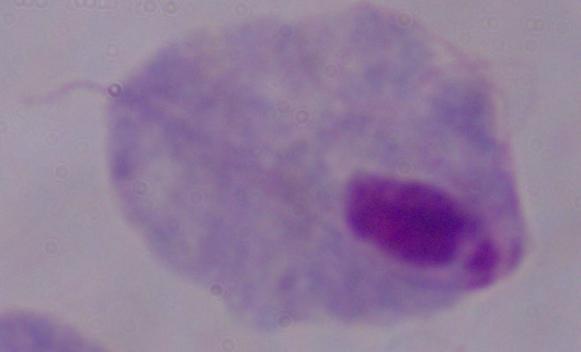
A trichomonad is seen. 1000x magnification. Photomicrograph.